Name the blood parasite species.
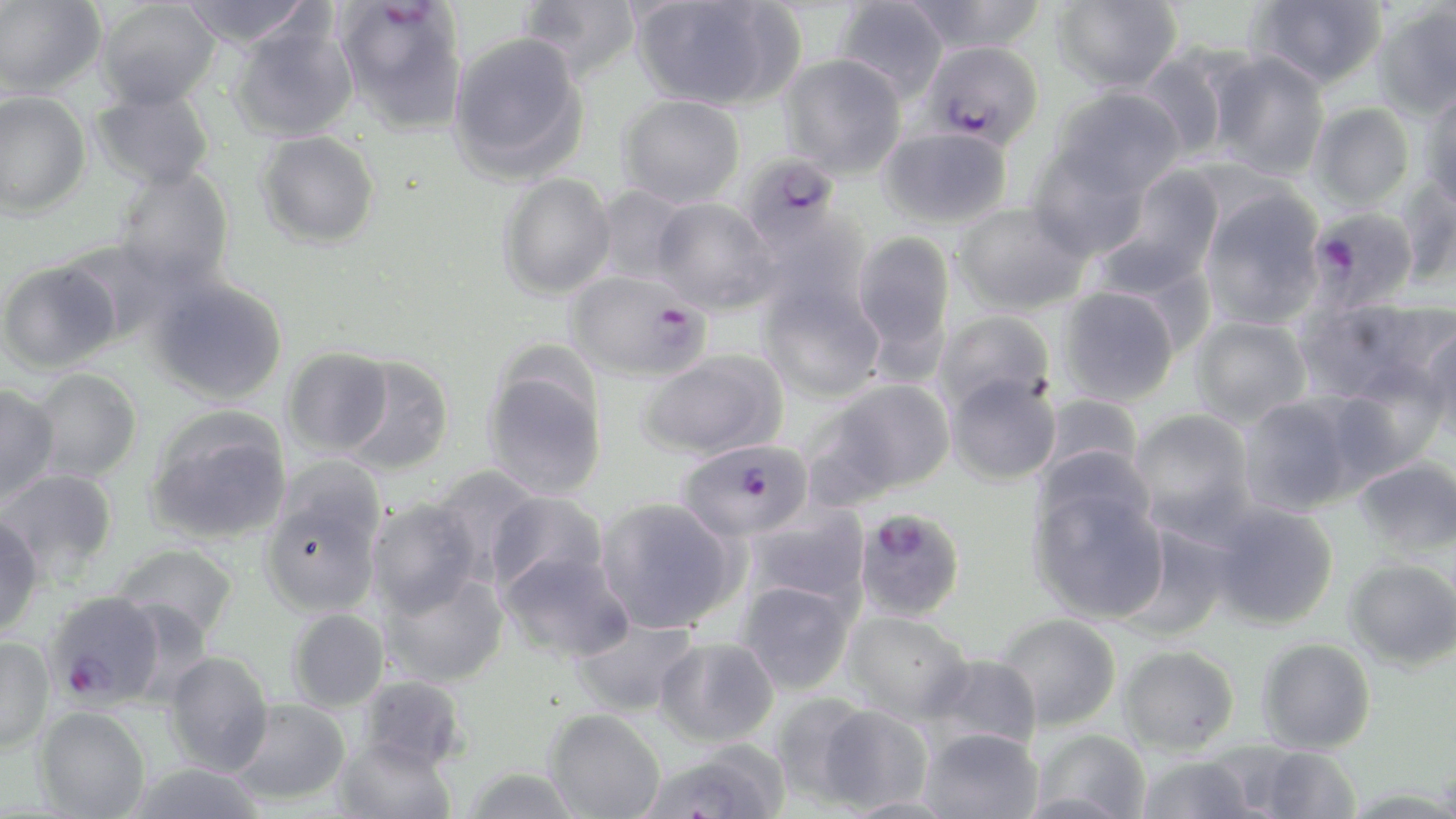

Plasmodium falciparum.

Summary:
  - Coordinate format: approximate bounding boxes as (x1, y1, x2, y2) in pixels
  - Plasmodium falciparum-infected red blood cell locations: (333, 1, 470, 135), (921, 40, 1044, 150), (735, 151, 839, 255), (1304, 207, 1419, 311), (566, 270, 710, 382), (677, 439, 813, 542), (852, 506, 966, 624), (43, 589, 167, 710)
  - Uninfected red blood cell locations: (0, 0, 106, 97), (177, 0, 318, 50), (517, 0, 643, 82), (834, 0, 950, 102), (901, 0, 1049, 55), (1051, 0, 1182, 93), (1249, 0, 1388, 89), (95, 1, 220, 110), (630, 1, 802, 112), (1371, 4, 1456, 122), (227, 16, 358, 144), (447, 31, 590, 184), (1134, 46, 1243, 161), (1207, 50, 1331, 181), (778, 53, 907, 179), (90, 85, 215, 191), (1050, 86, 1186, 197), (1419, 86, 1456, 213), (1, 91, 91, 219), (618, 94, 746, 208), (1308, 102, 1415, 210), (879, 126, 1012, 229), (255, 130, 381, 250), (1026, 146, 1150, 262), (112, 166, 235, 289), (1096, 166, 1227, 296), (497, 173, 616, 300), (1394, 178, 1456, 288), (594, 185, 693, 284), (1198, 186, 1326, 329), (651, 197, 778, 314), (953, 202, 1089, 316), (754, 212, 873, 322), (851, 231, 956, 364), (57, 239, 178, 345), (0, 259, 120, 374), (146, 273, 288, 406), (757, 277, 885, 404), (1057, 285, 1180, 407), (1298, 295, 1452, 405), (933, 309, 1057, 415), (1189, 316, 1312, 428), (1422, 319, 1456, 443), (282, 346, 393, 457), (637, 350, 788, 461), (337, 355, 455, 476), (482, 359, 608, 501), (29, 368, 143, 483), (1326, 368, 1450, 480), (945, 372, 1061, 486), (814, 377, 956, 500), (0, 383, 60, 503), (1036, 392, 1144, 486), (1237, 392, 1369, 517), (144, 406, 293, 545), (1129, 408, 1256, 534), (1353, 456, 1456, 557), (428, 464, 544, 580), (0, 467, 118, 580), (258, 477, 385, 618), (1027, 480, 1170, 625), (486, 491, 609, 598), (595, 496, 742, 632), (365, 497, 484, 616), (1207, 500, 1339, 630), (745, 506, 871, 611), (0, 513, 45, 638), (1113, 523, 1235, 641), (112, 542, 240, 641), (496, 549, 633, 663), (1344, 557, 1456, 671), (382, 570, 509, 687), (736, 579, 856, 696), (286, 608, 390, 712), (843, 609, 973, 723), (992, 613, 1122, 730), (568, 616, 700, 718), (0, 636, 54, 753), (654, 636, 779, 748), (1257, 638, 1376, 754), (1118, 644, 1240, 755), (163, 650, 275, 775), (929, 653, 1043, 752), (356, 674, 468, 772), (768, 693, 878, 807), (227, 698, 352, 806), (814, 703, 934, 814), (33, 705, 151, 818), (544, 708, 666, 819), (919, 727, 1043, 819), (1029, 730, 1150, 818), (333, 736, 456, 819), (640, 744, 788, 817), (1252, 745, 1363, 819), (1136, 754, 1257, 819), (124, 761, 268, 819), (460, 764, 583, 819)
  - Field of view: single
  - Image size: 1456×819 pixels
  - Preparation: thin blood film
  - Stain: May-Grünwald-Giemsa
  - Magnification: 1000x
  - Modality: optical microscopy